Give the extent of all Plasmodium falciparum-infected red blood cells.
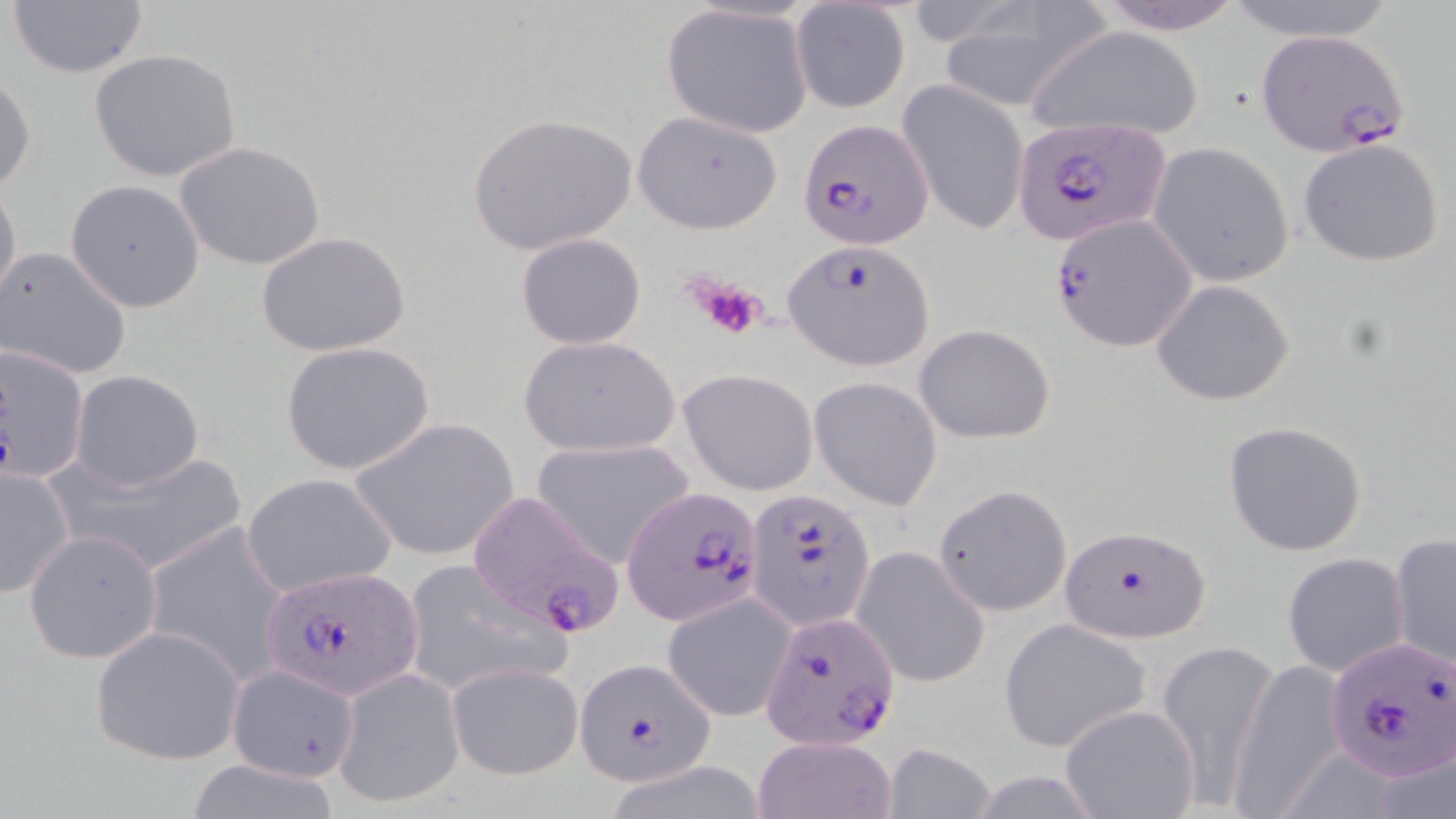

Approximate bounding boxes as (x1, y1, x2, y2) in pixels.
Plasmodium falciparum-infected red blood cells: (1251, 29, 1405, 157), (798, 118, 933, 249), (1010, 118, 1168, 246), (1049, 216, 1197, 351), (784, 240, 936, 371), (0, 347, 90, 483), (621, 483, 766, 627), (464, 489, 630, 639), (741, 490, 874, 629), (1060, 524, 1211, 642), (260, 566, 424, 696), (758, 608, 900, 751), (1328, 637, 1456, 782), (574, 656, 714, 785).

Summary:
  - Uninfected red blood cell locations: (7, 0, 152, 79), (1088, 0, 1250, 34), (1222, 0, 1403, 44), (789, 2, 911, 116), (938, 2, 1112, 114), (660, 3, 813, 138), (1025, 25, 1206, 143), (87, 48, 242, 182), (0, 71, 36, 194), (897, 77, 1029, 236), (466, 111, 639, 256), (632, 111, 783, 234), (1297, 137, 1445, 269), (174, 141, 325, 271), (1148, 142, 1294, 285), (0, 178, 22, 312), (65, 180, 204, 313), (259, 232, 411, 357), (515, 232, 648, 350), (0, 246, 133, 382), (1151, 279, 1293, 406), (913, 323, 1058, 444), (517, 335, 680, 457), (280, 340, 435, 477), (679, 368, 818, 495), (70, 369, 205, 492), (808, 377, 942, 511), (350, 417, 521, 563), (1222, 419, 1369, 557), (530, 439, 696, 567), (66, 446, 241, 580), (0, 465, 75, 598), (240, 474, 396, 598), (932, 486, 1075, 621), (140, 520, 292, 686), (22, 528, 164, 666), (1389, 532, 1455, 670), (852, 548, 990, 688), (1282, 552, 1412, 678), (400, 557, 570, 697), (663, 591, 796, 721), (999, 620, 1150, 752), (88, 625, 245, 765), (1153, 644, 1279, 805), (1228, 658, 1350, 814), (446, 661, 582, 781), (224, 663, 362, 785), (332, 667, 464, 807), (1058, 703, 1202, 819), (753, 736, 896, 819), (878, 743, 995, 819), (177, 759, 348, 817)
  - Platelet locations: (684, 270, 771, 344)
  - Slide-level diagnosis: Plasmodium falciparum
  - Modality: optical microscopy
  - Field of view: one of a larger specimen
  - Preparation: thin blood film
  - Stain: May-Grünwald-Giemsa
  - Magnification: 1000x
  - Image size: 1456×819 pixels